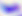
Summary:
  - Identification: Toxoplasma gondii
  - Modality: micrograph
  - Magnification: 400x